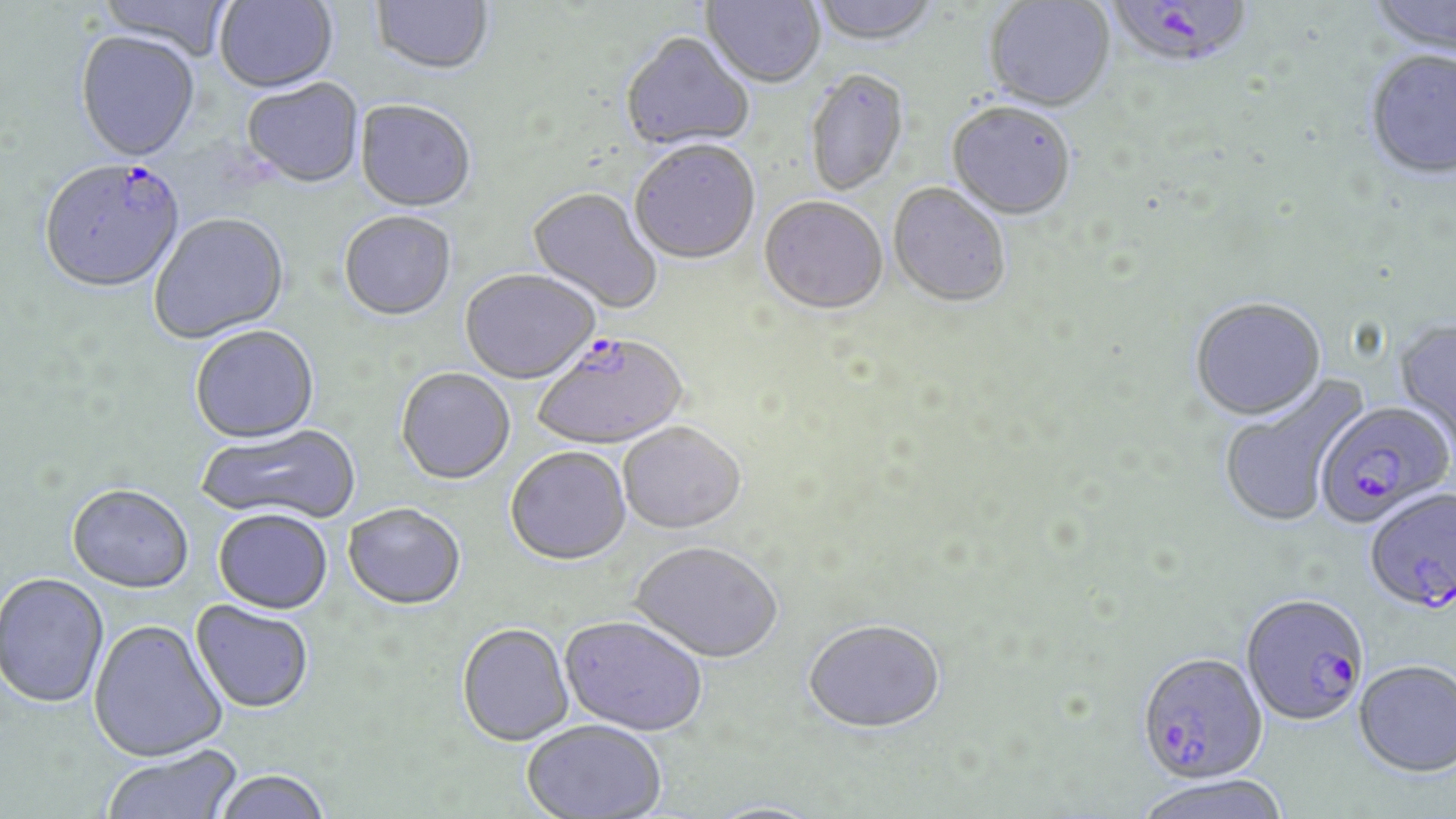
{
  "slide_level_diagnosis": "Plasmodium falciparum",
  "stain": "May-Grünwald-Giemsa",
  "field_of_view": "single",
  "modality": "optical microscopy",
  "uninfected_red_blood_cell_locations": "approximate bounding boxes as (x1,y1)-(x2,y2) corner pairs in pixels: (98,0)-(235,64), (214,0)-(339,95), (370,0)-(496,78), (701,0)-(825,90), (810,0)-(942,49), (1366,0)-(1456,60), (984,1)-(1115,114), (75,33)-(201,165), (620,35)-(754,153), (1364,53)-(1456,183), (805,71)-(909,198), (241,81)-(365,190), (354,101)-(477,214), (946,104)-(1076,222), (630,143)-(760,267), (888,185)-(1010,310), (526,188)-(662,315), (759,199)-(888,318), (339,213)-(457,323), (149,215)-(291,345), (460,270)-(600,386), (1189,299)-(1327,423), (1393,320)-(1456,458), (190,327)-(321,446), (396,369)-(515,486), (1218,375)-(1367,530), (196,425)-(362,526), (619,425)-(746,537), (505,449)-(631,568), (67,486)-(194,595), (343,505)-(466,612), (213,511)-(332,616), (629,545)-(782,666), (0,574)-(109,709), (190,601)-(314,714), (558,618)-(708,738), (88,620)-(228,763), (804,622)-(945,737), (456,625)-(573,748), (1354,659)-(1456,778), (522,722)-(666,817), (101,744)-(243,819), (213,771)-(331,819), (1131,775)-(1293,819)",
  "magnification": "1000x",
  "image_size": "1456×819 pixels",
  "preparation": "thin blood smear",
  "plasmodium_falciparum_infected_red_blood_cell_locations": "approximate bounding boxes as (x1,y1)-(x2,y2) corner pairs in pixels: (1107,0)-(1253,74), (38,161)-(187,297), (533,335)-(689,453), (1314,402)-(1454,530), (1365,488)-(1456,616), (1241,596)-(1368,728), (1136,654)-(1267,785)"
}